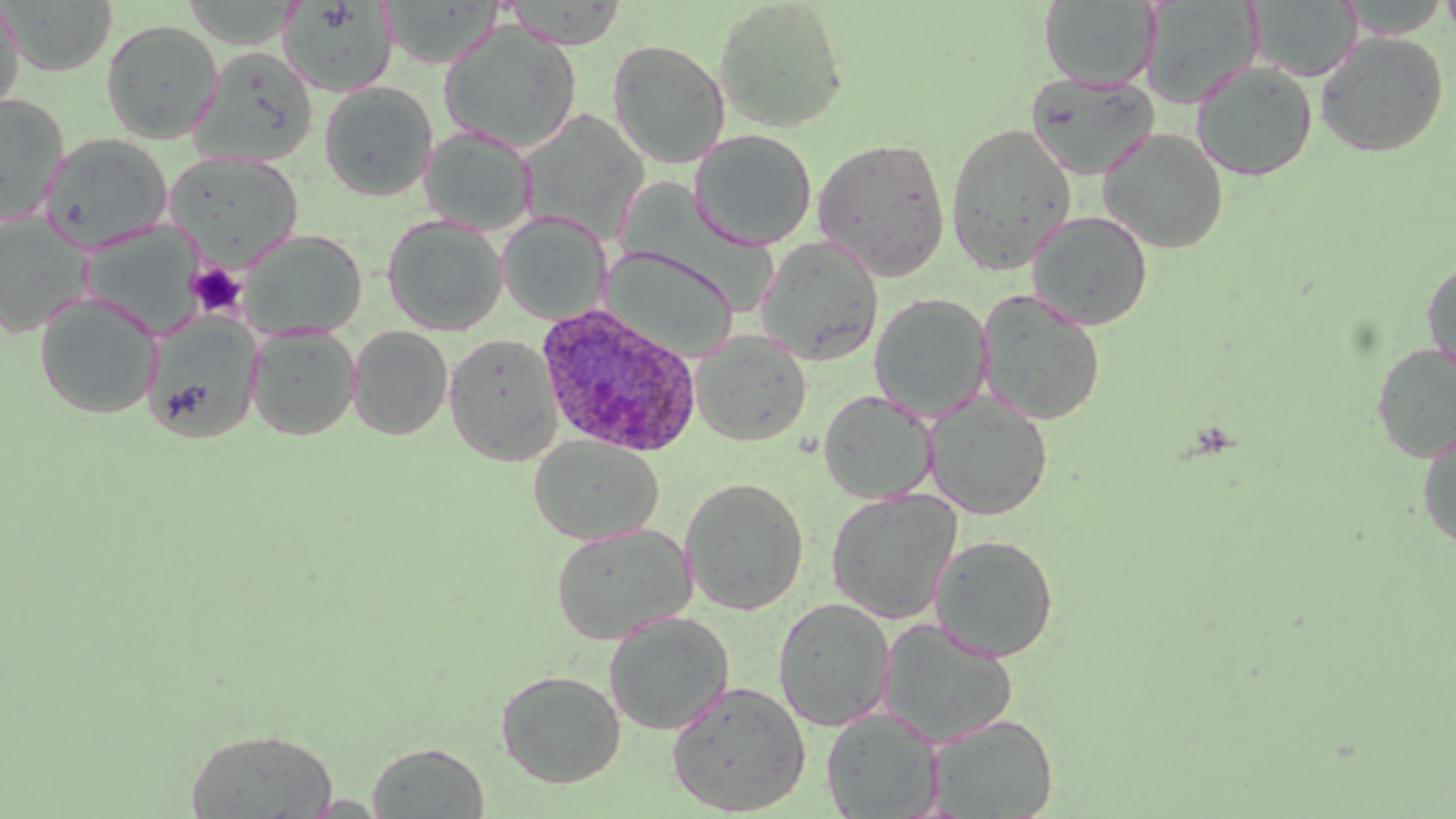

Summary:
  - Coordinate format: approximate bounding boxes as (x1,y1)-(x2,y2) corner pairs in pixels
  - Plasmodium ovale-infected red blood cell locations: (536,303)-(702,459)
  - Uninfected red blood cell locations: (713,0)-(850,134), (1335,0)-(1452,39), (1439,0)-(1456,42), (1,1)-(117,76), (182,1)-(305,49), (279,1)-(399,97), (503,1)-(629,49), (1039,1)-(1161,90), (1140,1)-(1264,109), (1249,1)-(1362,81), (0,2)-(25,118), (101,20)-(223,143), (438,21)-(583,155), (1314,31)-(1449,157), (607,39)-(731,168), (190,47)-(318,166), (1191,61)-(1318,181), (1026,72)-(1160,181), (319,82)-(438,201), (0,94)-(69,226), (518,109)-(649,242), (945,122)-(1078,275), (419,125)-(537,236), (1097,128)-(1230,253), (688,129)-(817,251), (40,132)-(173,252), (813,137)-(951,282), (164,152)-(304,270), (1027,210)-(1153,331), (497,211)-(612,325), (0,213)-(94,337), (382,215)-(507,336), (79,220)-(207,338), (238,228)-(367,341), (755,236)-(884,366), (600,246)-(737,361), (1422,258)-(1456,382), (975,289)-(1106,426), (34,292)-(161,419), (869,293)-(993,420), (141,313)-(263,444), (348,325)-(453,440), (247,327)-(360,441), (690,329)-(812,446), (444,333)-(564,466), (1371,342)-(1456,462), (819,390)-(937,504), (924,392)-(1053,520), (1417,431)-(1456,552), (529,435)-(664,546), (680,476)-(809,615), (826,489)-(963,625), (551,523)-(696,646), (930,534)-(1059,663), (773,597)-(895,732), (603,611)-(734,735), (877,618)-(1018,748), (496,669)-(626,788), (665,680)-(811,817), (821,707)-(945,818), (925,714)-(1058,818), (185,729)-(338,818), (367,742)-(489,818), (300,794)-(388,817)
  - Platelet locations: (187,263)-(247,318)
  - Slide-level diagnosis: Plasmodium ovale
  - Field of view: one of a larger specimen
  - Modality: light microscopy
  - Preparation: thin blood film
  - Stain: May-Grünwald-Giemsa
  - Image size: 1456×819 pixels
  - Magnification: 1000x